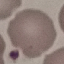 Malaria status: uninfected. Thin blood smear. Automatically extracted cell patch, resized to 64 × 64 pixels. Photographed with a smartphone camera at the microscope eyepiece. Giemsa stain.